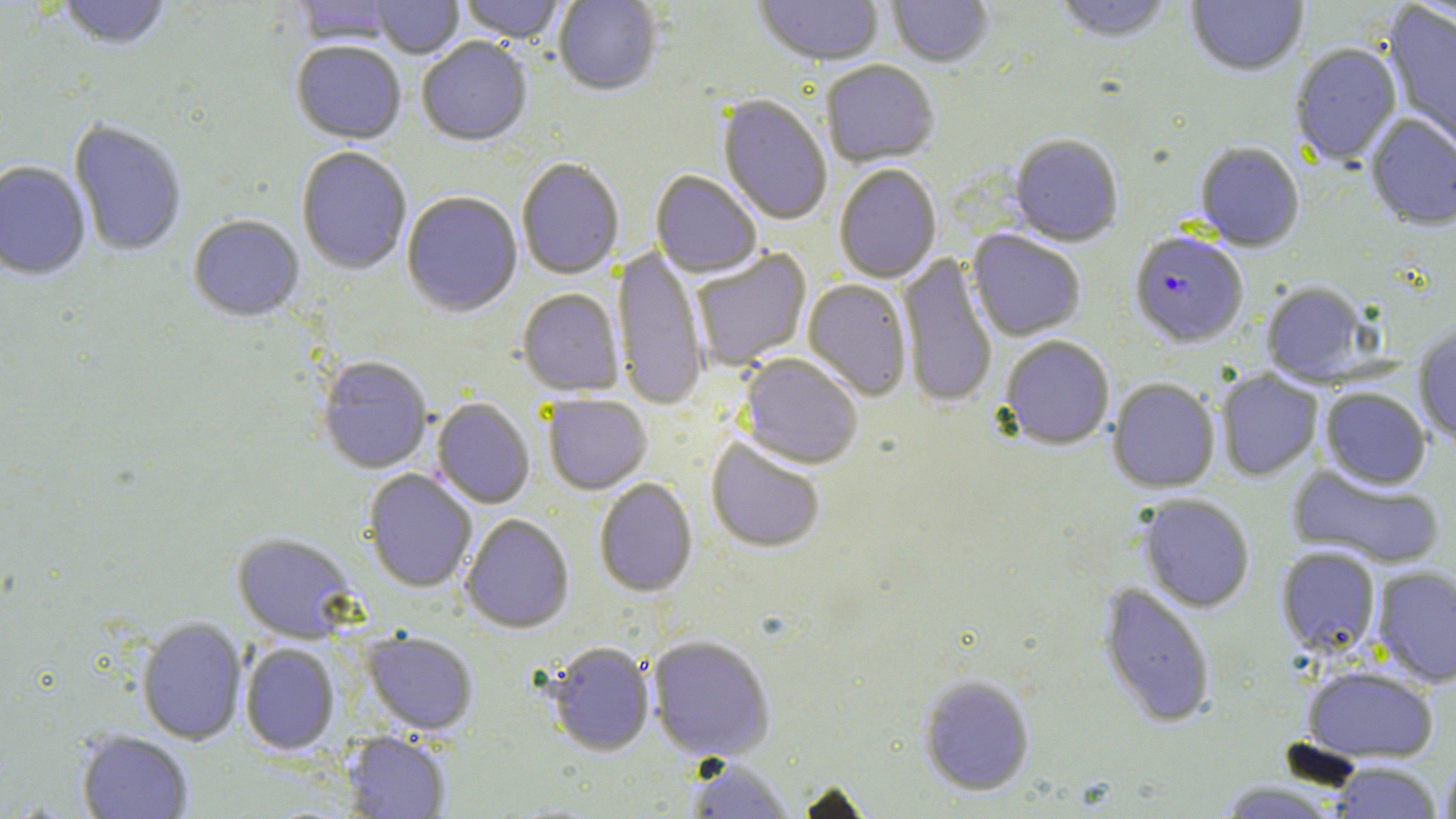
Summary:
  - Coordinate format: approximate bounding boxes as named x1/y1/x2/y2 corners in pixels
  - Plasmodium falciparum-infected red blood cell locations: (x1=1129, y1=232, x2=1249, y2=348)
  - Uninfected red blood cell locations: (x1=56, y1=0, x2=172, y2=52), (x1=293, y1=0, x2=399, y2=48), (x1=370, y1=0, x2=464, y2=60), (x1=459, y1=0, x2=565, y2=45), (x1=553, y1=0, x2=661, y2=98), (x1=753, y1=0, x2=884, y2=68), (x1=887, y1=0, x2=994, y2=70), (x1=1053, y1=0, x2=1173, y2=45), (x1=1186, y1=0, x2=1308, y2=78), (x1=1382, y1=4, x2=1456, y2=155), (x1=417, y1=39, x2=532, y2=148), (x1=291, y1=43, x2=406, y2=146), (x1=1290, y1=44, x2=1402, y2=168), (x1=821, y1=61, x2=939, y2=168), (x1=717, y1=95, x2=832, y2=226), (x1=1365, y1=115, x2=1456, y2=233), (x1=69, y1=121, x2=187, y2=259), (x1=1009, y1=136, x2=1123, y2=248), (x1=1194, y1=144, x2=1304, y2=252), (x1=296, y1=148, x2=412, y2=276), (x1=517, y1=160, x2=624, y2=280), (x1=0, y1=162, x2=91, y2=282), (x1=834, y1=166, x2=942, y2=284), (x1=650, y1=171, x2=762, y2=279), (x1=402, y1=193, x2=523, y2=319), (x1=188, y1=216, x2=304, y2=323), (x1=967, y1=230, x2=1085, y2=341), (x1=613, y1=244, x2=709, y2=411), (x1=690, y1=248, x2=812, y2=371), (x1=897, y1=253, x2=998, y2=410), (x1=803, y1=279, x2=913, y2=402), (x1=1261, y1=283, x2=1374, y2=386), (x1=517, y1=290, x2=624, y2=397), (x1=1413, y1=324, x2=1456, y2=446), (x1=1000, y1=336, x2=1115, y2=451), (x1=738, y1=353, x2=863, y2=470), (x1=317, y1=357, x2=433, y2=474), (x1=1215, y1=369, x2=1323, y2=481), (x1=1107, y1=379, x2=1220, y2=493), (x1=1320, y1=388, x2=1431, y2=489), (x1=542, y1=395, x2=652, y2=495), (x1=431, y1=398, x2=535, y2=509), (x1=706, y1=436, x2=826, y2=553), (x1=1287, y1=465, x2=1444, y2=568), (x1=362, y1=469, x2=477, y2=593), (x1=594, y1=479, x2=698, y2=597), (x1=1137, y1=495, x2=1255, y2=613), (x1=460, y1=514, x2=574, y2=634), (x1=232, y1=533, x2=358, y2=644), (x1=1276, y1=547, x2=1381, y2=656), (x1=1372, y1=566, x2=1456, y2=686), (x1=1098, y1=583, x2=1215, y2=728), (x1=137, y1=618, x2=247, y2=745), (x1=362, y1=631, x2=478, y2=736), (x1=647, y1=635, x2=775, y2=762), (x1=546, y1=642, x2=656, y2=757), (x1=240, y1=643, x2=339, y2=756), (x1=1302, y1=665, x2=1438, y2=763), (x1=918, y1=676, x2=1035, y2=796), (x1=76, y1=731, x2=193, y2=818), (x1=343, y1=732, x2=451, y2=818), (x1=1440, y1=754, x2=1456, y2=819), (x1=687, y1=759, x2=793, y2=818), (x1=1329, y1=762, x2=1442, y2=819), (x1=795, y1=781, x2=876, y2=818), (x1=1216, y1=781, x2=1342, y2=818)
  - Slide-level diagnosis: Plasmodium falciparum
  - Field of view: single
  - Image size: 1456×819 pixels
  - Preparation: thin blood film
  - Magnification: 1000x
  - Stain: May-Grünwald-Giemsa
  - Modality: light microscopy